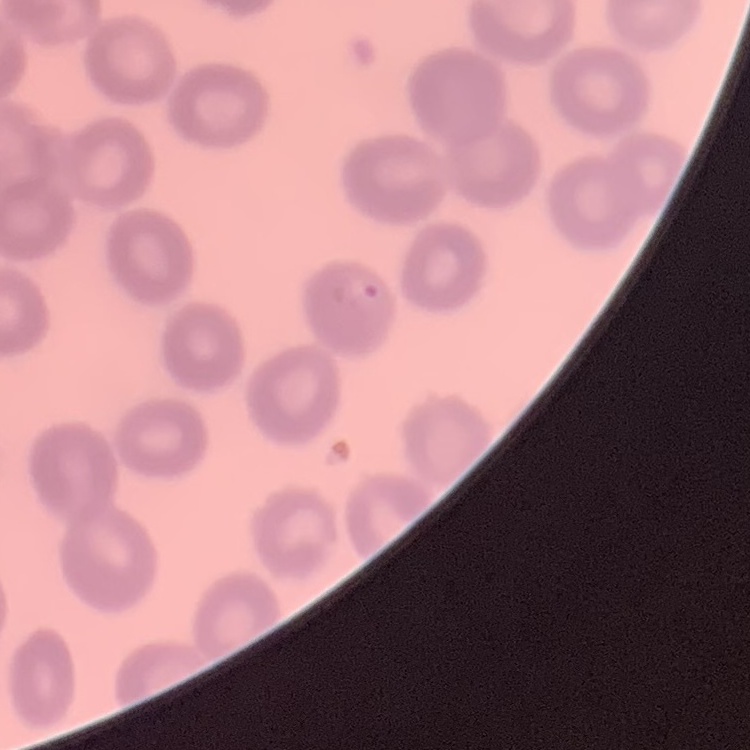
The erythrocytes exhibit no rouleaux formation. Field's or Giemsa stain. Square crop of a larger photomicrograph. Thin blood film.